Describe the morphology of the red blood cells.
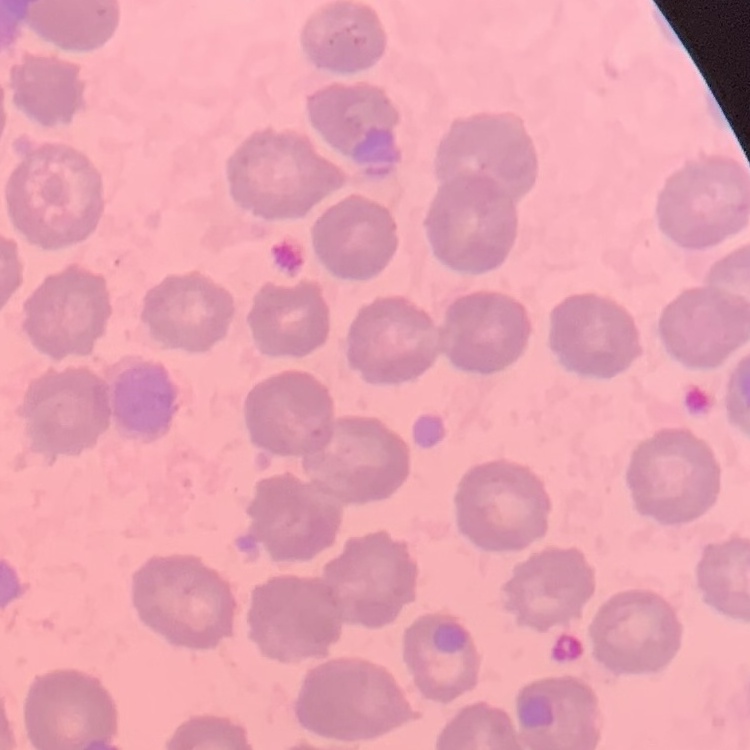

No rouleaux formation.

Summary:
  - Preparation: thin blood film
  - Stain: Field's or Giemsa
  - Image type: one tile cut from a larger photomicrograph